Classify this cell by malaria status.
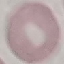

Uninfected.

Automatically extracted cell patch, resized to 64 × 64 pixels. Thin blood smear. Acquired by smartphone through the microscope eyepiece. Giemsa stain.